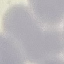
Summary:
  - Malaria status: uninfected
  - Preparation: thin blood film
  - Stain: Giemsa
  - Capture: smartphone camera at the microscope eyepiece
  - Image type: automatically extracted cell patch, resized to 64 × 64 pixels